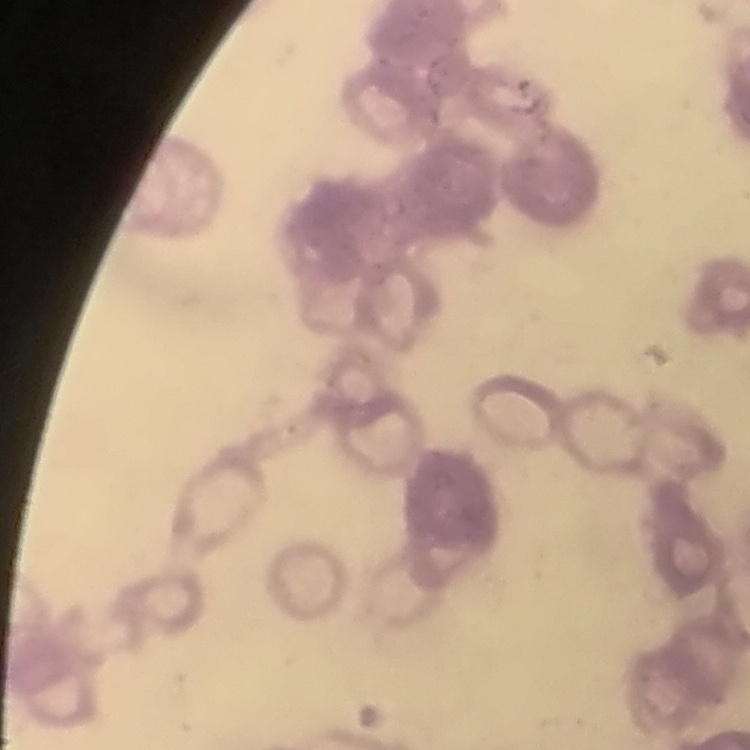
Summary:
  - Red blood cell morphology: rouleaux formation
  - Image type: square crop of a larger photomicrograph
  - Preparation: thin blood smear
  - Stain: Field's or Giemsa